Describe the morphology of the erythrocytes.
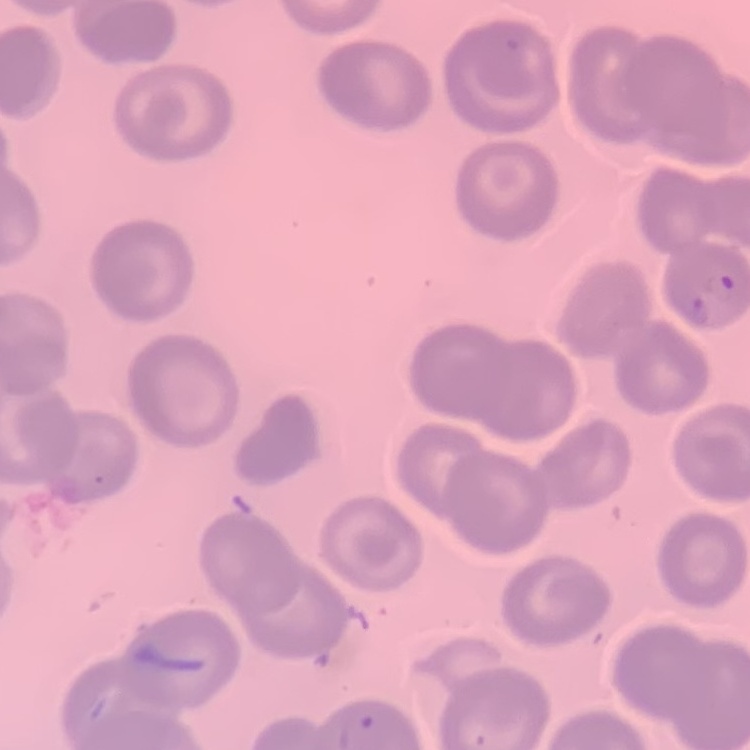

No rouleaux formation.

Summary:
  - Image type: square crop of a larger photomicrograph
  - Stain: Field's or Giemsa
  - Preparation: thin blood smear